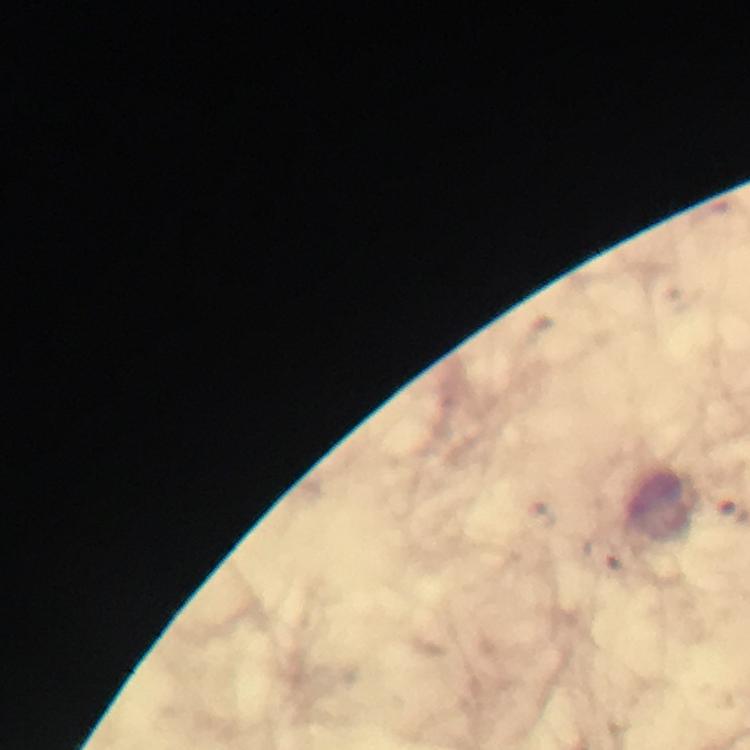
Approximate centers as [x, y] in pixels.
Summary:
  - Plasmodium parasite locations: [605, 554]
  - Magnification: 100x
  - Image size: 750×750 pixels
  - Immersion oil: used
  - Context: from a malaria diagnostic workup
  - Cropped from: one field of view
  - Capture: smartphone camera through the microscope
  - Preparation: thick blood film
  - Stain: Giemsa